Give the preparation type.
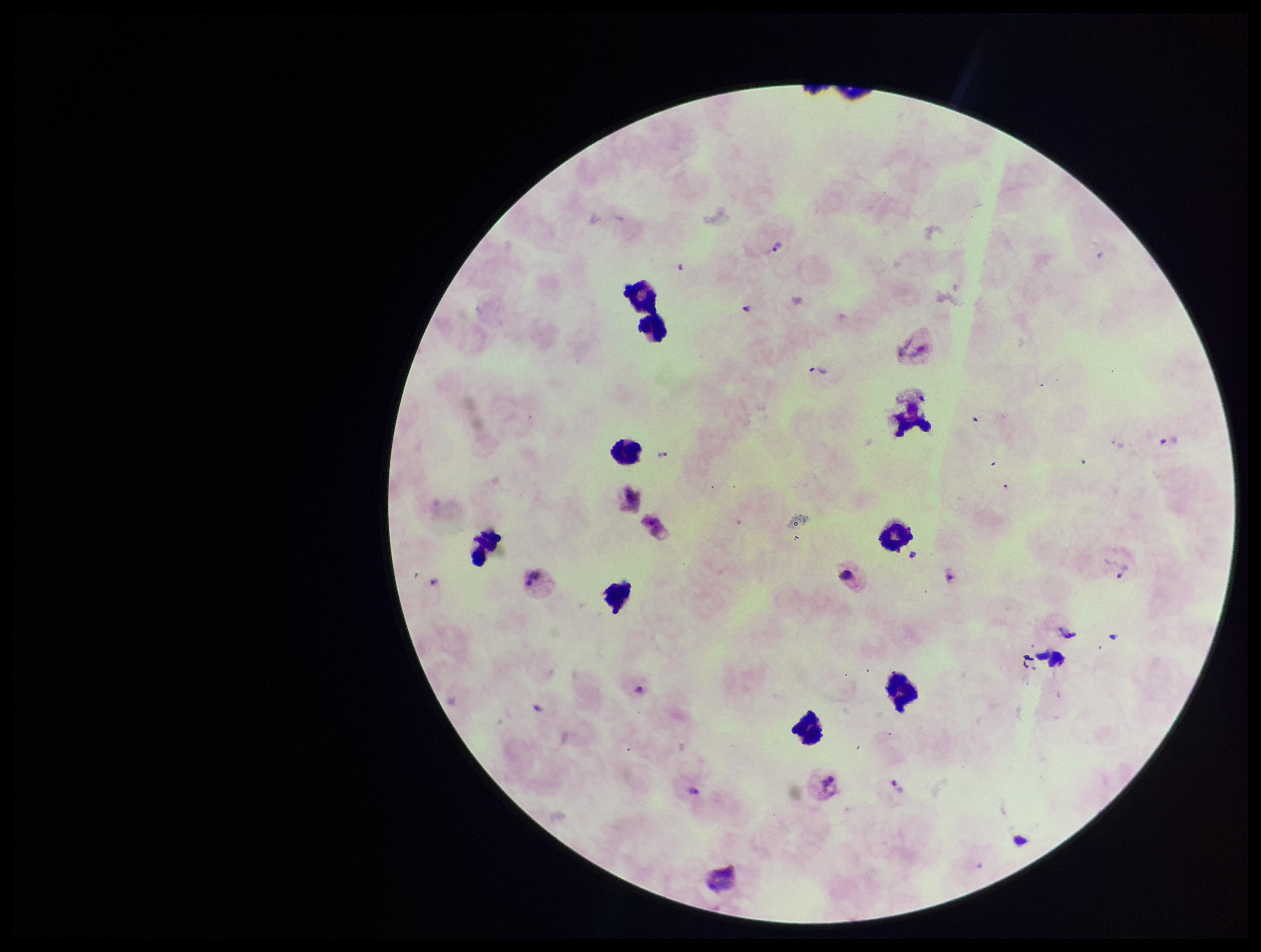
It is a thick blood smear.

Parasite count: 10. Smartphone photograph taken through the eyepiece of a microscope. Patient malaria status: positive. One field from this slide. Image is 1261×952 pixels. Leukocyte count: 9. Plasmodium parasites: seen. Giemsa stain. Species reported for this patient: Plasmodium vivax.